Identify the parasite.
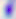
This is Toxoplasma gondii.

Summary:
  - Modality: photomicrograph
  - Magnification: 400x